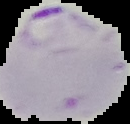
{
  "image_type": "segmented cell region with the area outside set to black",
  "image_size": "130×124 pixels",
  "result": "Plasmodium parasites detected",
  "preparation": "thin blood film"
}